Classify this cell by malaria status.
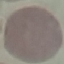

It is uninfected.

{
  "capture": "smartphone camera at the microscope eyepiece",
  "preparation": "thin smear",
  "image_type": "cell patch, automatically extracted from a larger field of view and resized to 64 × 64 pixels",
  "stain": "Giemsa"
}